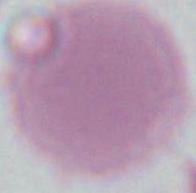

{
  "modality": "photomicrograph",
  "magnification": "1000x",
  "identification": "red blood cell"
}